Evaluate for Plasmodium parasites.
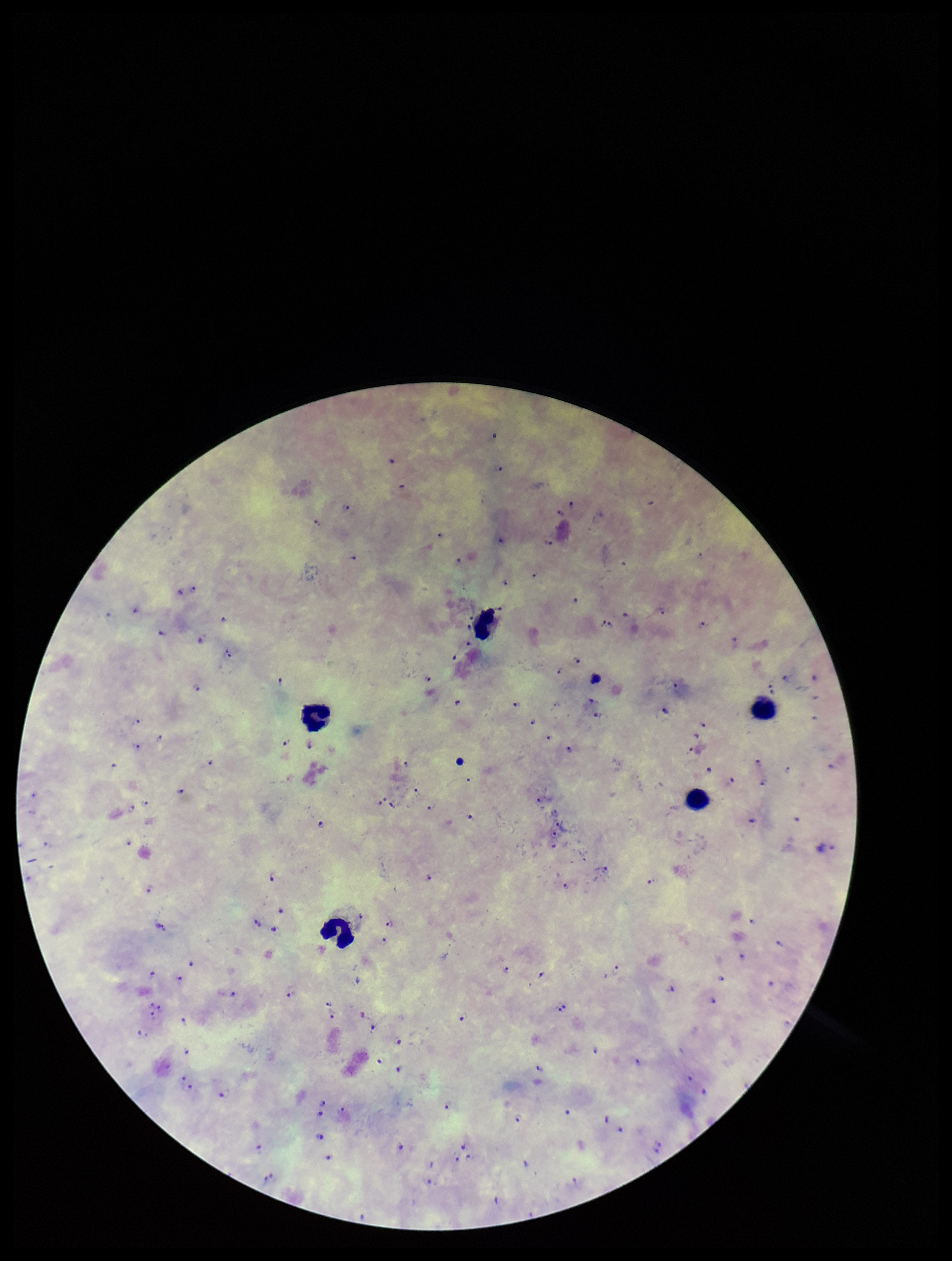

Seen.

Summary:
  - Preparation: thick smear
  - Field of view: one from this slide
  - Species reported for this patient: Plasmodium falciparum
  - Stain: Giemsa
  - Leukocyte count: 5
  - Image size: 952×1261 pixels
  - Capture: smartphone photograph through the microscope eyepiece
  - Parasite count: 101
  - Patient malaria status: positive